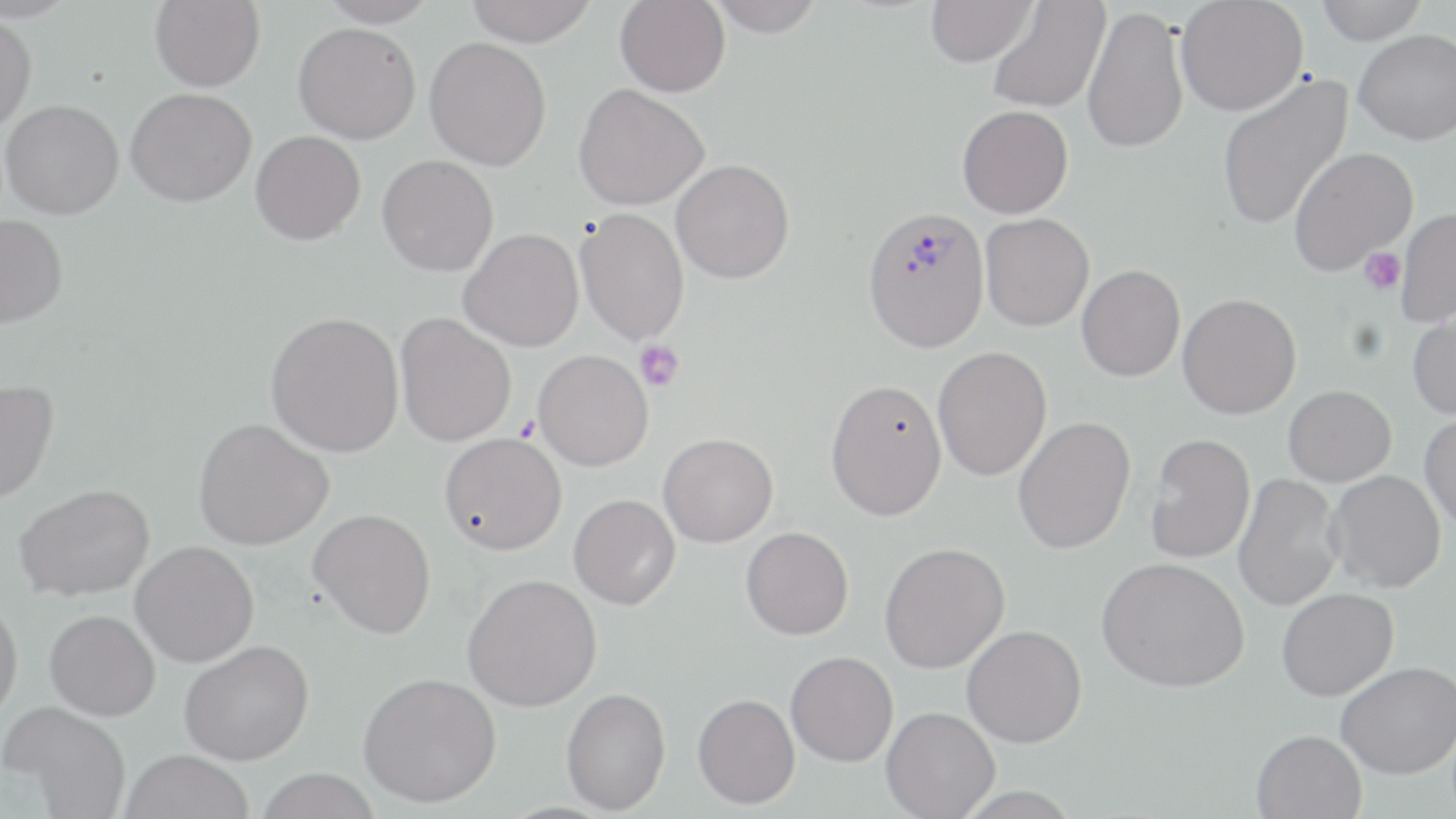

slide-level diagnosis = Plasmodium vivax
field of view = one of a larger specimen
platelet locations = approximate bounding boxes as (x1,y1)-(x2,y2) corner pairs in pixels: (1358,248)-(1406,295), (635,340)-(684,391)
image size = 1456×819 pixels
Plasmodium vivax-infected red blood cell locations = approximate bounding boxes as (x1,y1)-(x2,y2) corner pairs in pixels: (861,204)-(991,352)
preparation = thin blood smear
magnification = 1000x
stain = May-Grünwald-Giemsa
modality = light microscopy
uninfected red blood cell locations = approximate bounding boxes as (x1,y1)-(x2,y2) corner pairs in pixels: (150,0)-(265,92), (317,0)-(440,27), (465,0)-(598,46), (615,0)-(730,97), (925,0)-(1036,67), (1175,0)-(1309,116), (1314,0)-(1428,44), (704,1)-(826,37), (987,1)-(1110,113), (1082,5)-(1189,154), (0,13)-(37,131), (293,22)-(420,144), (1354,29)-(1456,144), (424,37)-(551,170), (1216,74)-(1354,232), (573,83)-(708,211), (126,88)-(256,207), (1,100)-(124,220), (957,105)-(1073,218), (251,130)-(365,245), (1288,147)-(1417,276), (377,155)-(498,277), (671,159)-(794,283), (574,208)-(689,345), (1396,208)-(1456,328), (980,213)-(1094,331), (0,214)-(68,330), (458,228)-(583,351), (1076,264)-(1185,381), (1178,293)-(1302,419), (1408,304)-(1456,421), (265,311)-(404,458), (395,312)-(516,447), (932,346)-(1052,482), (533,349)-(653,471), (825,378)-(947,520), (0,380)-(58,504), (1283,385)-(1396,486), (1419,413)-(1456,533), (1013,416)-(1136,554), (193,418)-(333,550), (439,431)-(567,555), (1145,432)-(1256,563), (659,433)-(778,547), (1326,469)-(1446,593), (1233,473)-(1345,612), (14,484)-(157,601), (569,494)-(680,610), (308,508)-(436,639), (741,526)-(854,639), (130,540)-(259,667), (879,542)-(1009,673), (1097,556)-(1250,692), (463,573)-(602,710), (1277,587)-(1399,701), (0,597)-(23,726), (45,610)-(160,720), (962,625)-(1087,748), (179,640)-(314,765), (786,651)-(898,767), (1336,661)-(1456,779), (358,671)-(501,808), (560,687)-(671,815), (692,693)-(800,809), (1,702)-(132,819), (881,706)-(999,819), (1251,729)-(1366,819), (119,749)-(254,819), (254,768)-(383,819)